State which cell type is depicted.
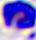
This is a leukocyte.

modality: micrograph
magnification: 400x